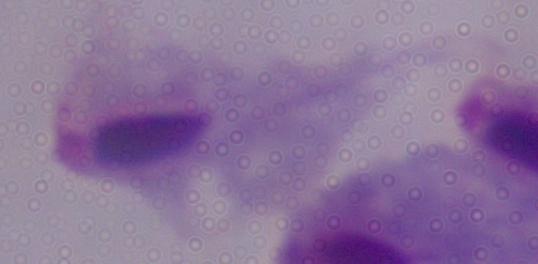 Micrograph. Captured at 1000x magnification. A trichomonad is shown.